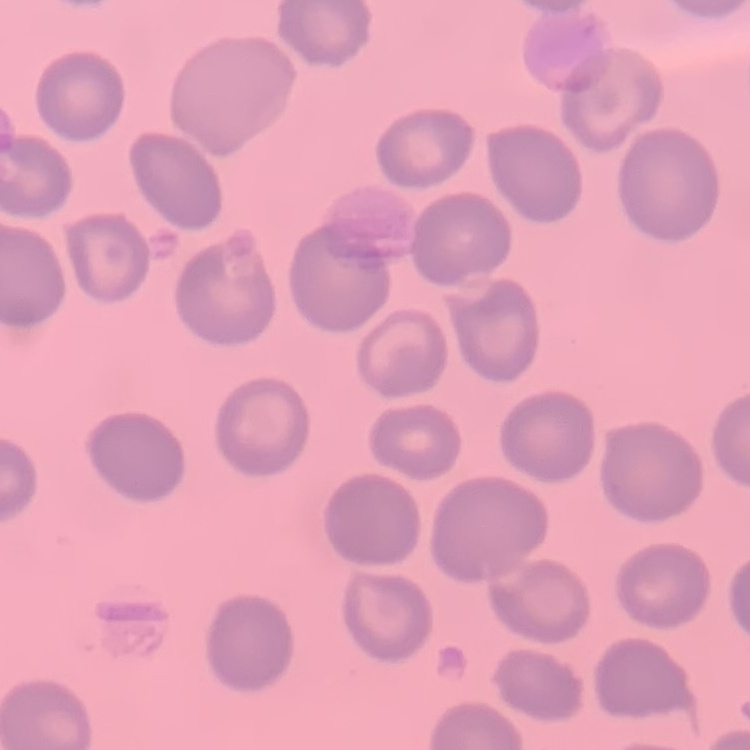

{
  "red_blood_cell_morphology": "no rouleaux formation",
  "stain": "Field's or Giemsa",
  "preparation": "thin blood film",
  "image_type": "square crop of a larger photomicrograph"
}